Identify the cell.
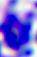
A leukocyte.

Summary:
  - Magnification: 400x
  - Modality: micrograph